Assess this cell for malaria.
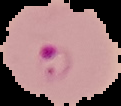
It is parasitized.

image type = segmented cell region on a black background
preparation = thin blood film
image size = 121×106 pixels